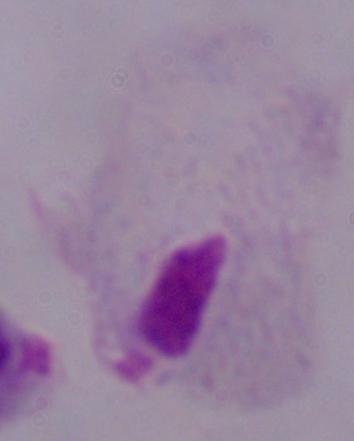 Captured at 1000x magnification. Photomicrograph. A trichomonad is shown.